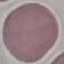

Summary:
  - Malaria status: uninfected
  - Stain: Giemsa
  - Image type: automatically extracted cell patch, resized to 64 × 64 pixels
  - Preparation: thin blood smear
  - Capture: smartphone through the microscope eyepiece